Assess this cell for malaria.
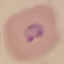
It is parasitized.

{
  "image_type": "automatically extracted cell patch, resized to 64 × 64 pixels",
  "stain": "Giemsa",
  "preparation": "thin smear",
  "capture": "smartphone through the microscope eyepiece"
}